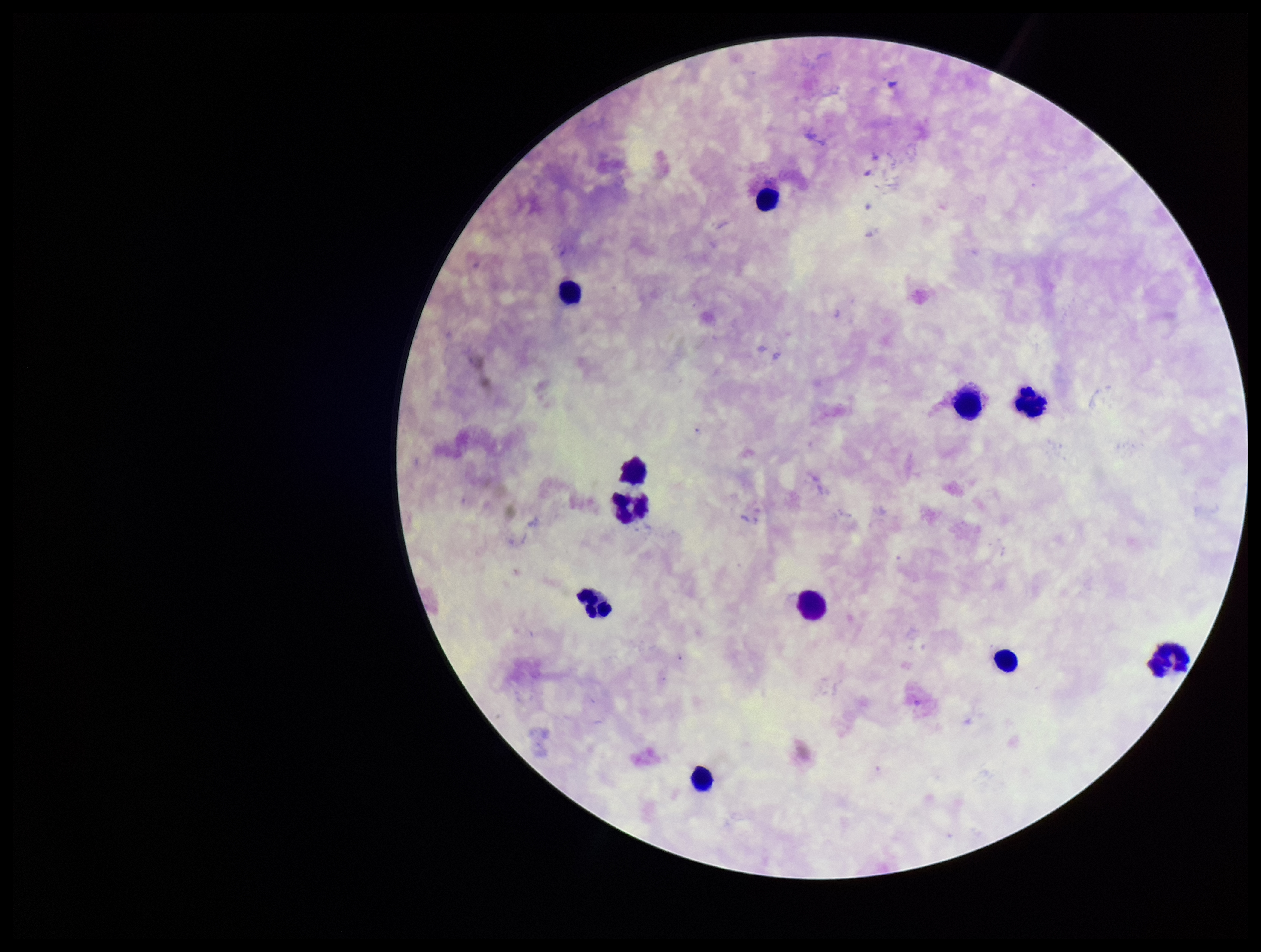

parasite count = 0
patient malaria status = negative
capture = smartphone photograph through the microscope eyepiece
field of view = one from this slide
stain = Giemsa
Plasmodium parasites = none seen
image size = 1261×952 pixels
preparation = thick smear
leukocyte count = 11